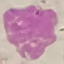
result = no malaria parasites seen
preparation = thin smear
capture = smartphone through the microscope eyepiece
image type = automatically extracted cell patch, resized to 64 × 64 pixels
stain = Giemsa